Name the cell type shown.
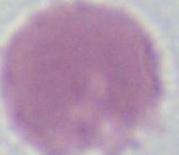

This is an erythrocyte.

Photomicrograph. Captured at 1000x magnification.